State the blood parasite species.
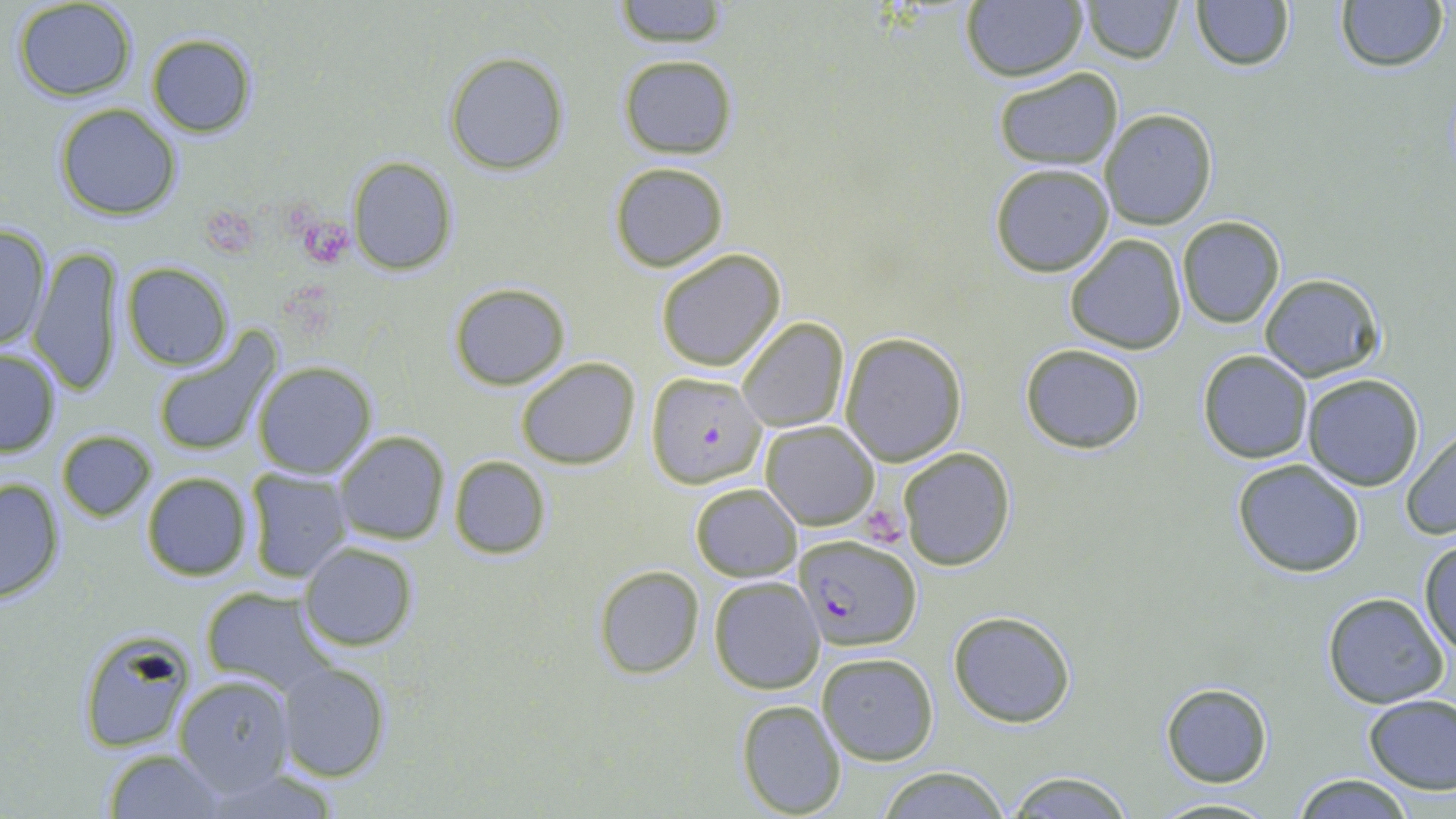

Plasmodium falciparum.

Approximate bounding boxes as (x1,y1)-(x2,y2) corner pairs in pixels. Plasmodium falciparum-infected red blood cell locations: (646,371)-(767,488), (793,534)-(921,651). Platelet locations: (196,202)-(264,261), (303,223)-(350,265), (865,506)-(904,552). Uninfected red blood cell locations: (612,0)-(731,47), (1079,0)-(1182,63), (12,1)-(138,101), (1189,1)-(1295,73), (1333,1)-(1448,74), (960,2)-(1086,82), (144,32)-(257,137), (442,52)-(570,176), (618,54)-(738,159), (992,66)-(1122,170), (54,102)-(182,221), (1100,109)-(1218,229), (350,156)-(459,275), (609,161)-(728,272), (988,163)-(1114,278), (1176,217)-(1286,328), (0,221)-(52,355), (1065,232)-(1186,355), (30,244)-(125,396), (655,248)-(785,372), (122,263)-(233,369), (1258,273)-(1385,382), (448,283)-(573,390), (736,318)-(849,434), (150,332)-(281,458), (838,332)-(969,466), (1019,343)-(1146,455), (0,347)-(63,458), (1196,350)-(1313,464), (516,357)-(640,469), (252,363)-(377,479), (1301,374)-(1426,492), (761,422)-(880,530), (1401,428)-(1456,540), (56,430)-(155,522), (333,430)-(450,545), (898,447)-(1015,570), (447,456)-(550,560), (1231,459)-(1365,578), (243,467)-(354,582), (141,472)-(252,581), (0,475)-(67,604), (691,483)-(801,582), (1419,538)-(1456,661), (300,541)-(418,650), (593,565)-(704,679), (709,575)-(825,694), (199,588)-(332,696), (1322,592)-(1448,709), (948,609)-(1077,728), (77,633)-(195,755), (817,652)-(939,766), (279,661)-(390,782), (174,673)-(297,798), (1160,683)-(1272,786), (1363,692)-(1456,794), (736,698)-(847,818), (103,747)-(224,818), (877,766)-(1010,819), (1003,769)-(1135,818), (1292,774)-(1418,818), (1148,795)-(1279,817). One field of a larger specimen. May-Grünwald-Giemsa stain. Image is 1456×819 pixels. Optical microscopy. 1000x magnification. Thin blood film.